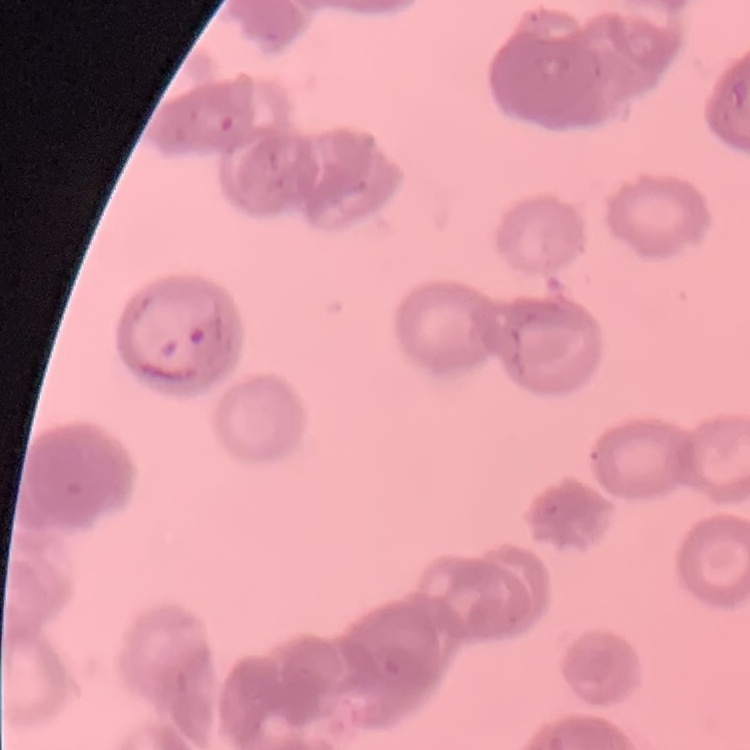

erythrocyte morphology = rouleaux formation
image type = square crop of a larger photomicrograph
preparation = thin blood film
stain = Field's or Giemsa